Assess for malaria.
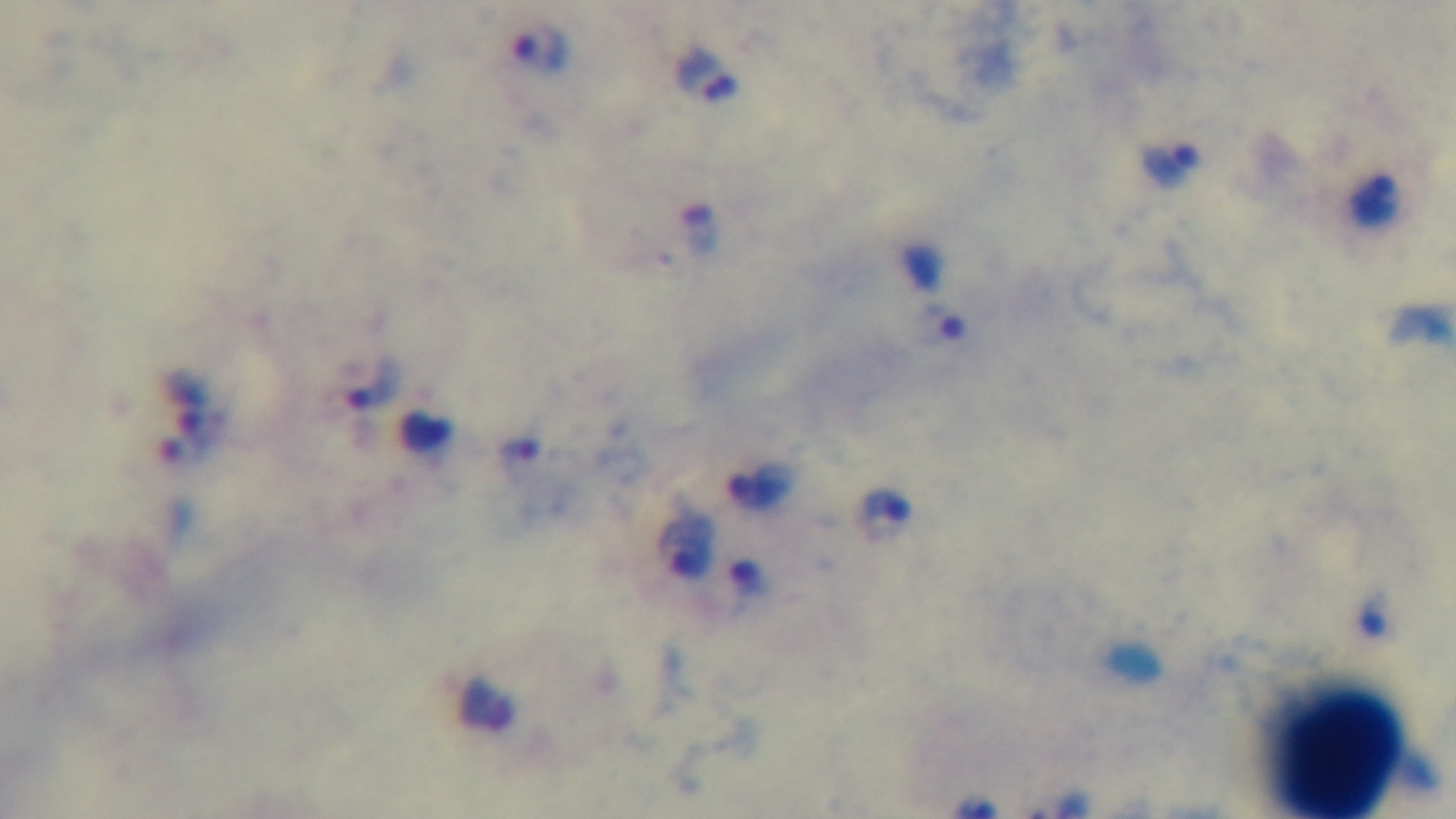
It is infected.

Summary:
  - Preparation: thick blood film
  - Modality: light microscopy
  - Stain: Giemsa
  - Objective: 100x oil immersion
  - Capture: mounted 4K digital camera
  - Field of view: one from the slide